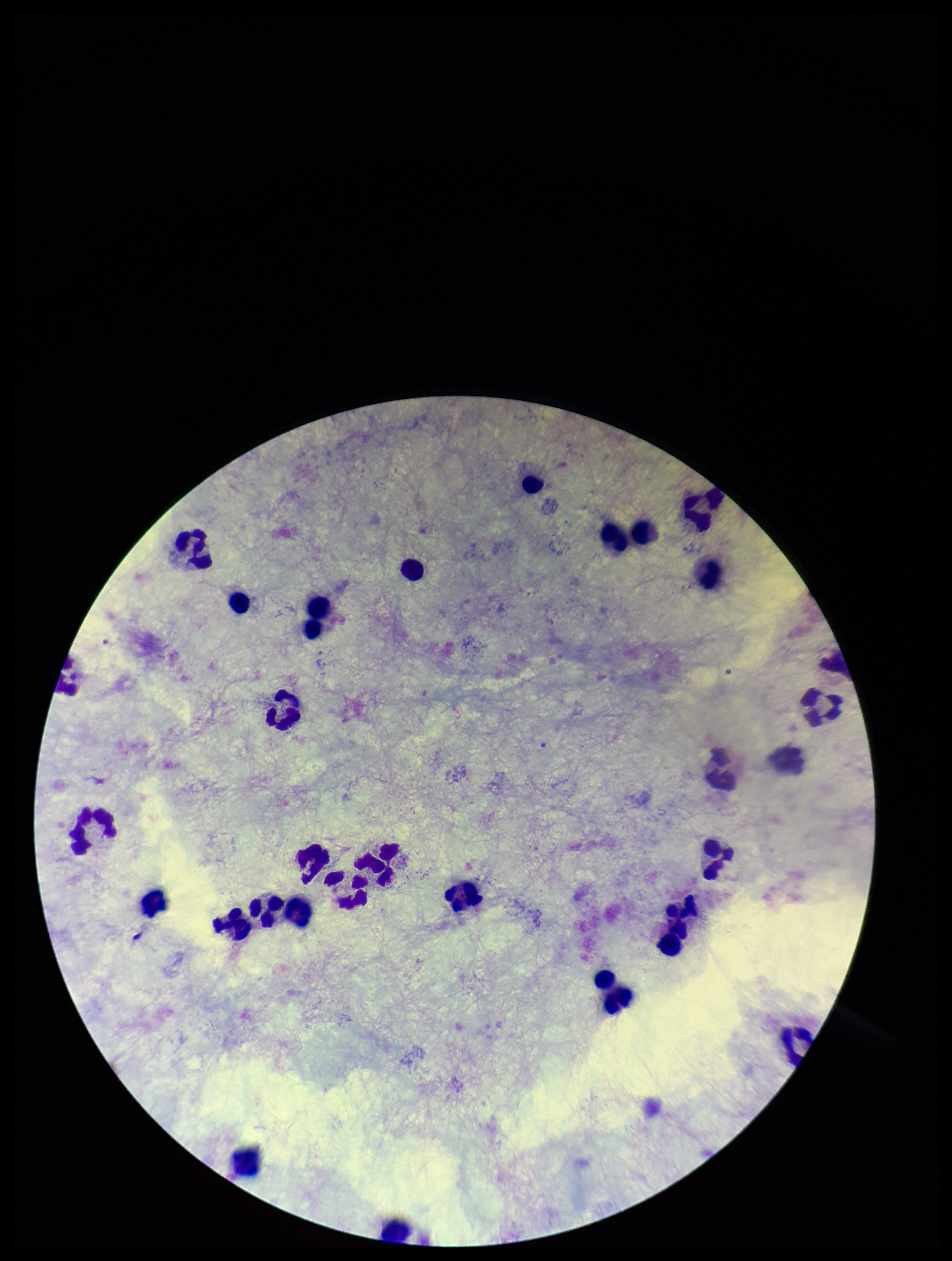

stain = Giemsa
preparation = thick
parasite count = 0
image size = 952×1261 pixels
field of view = one from this slide
capture = smartphone photograph through the microscope eyepiece
leukocyte count = 30
Plasmodium parasites = none seen
patient malaria status = negative